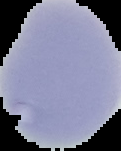
image type = segmented cell region with the area outside set to black
preparation = thin blood film
malaria status = uninfected
image size = 121×151 pixels